Identify the blood parasite species.
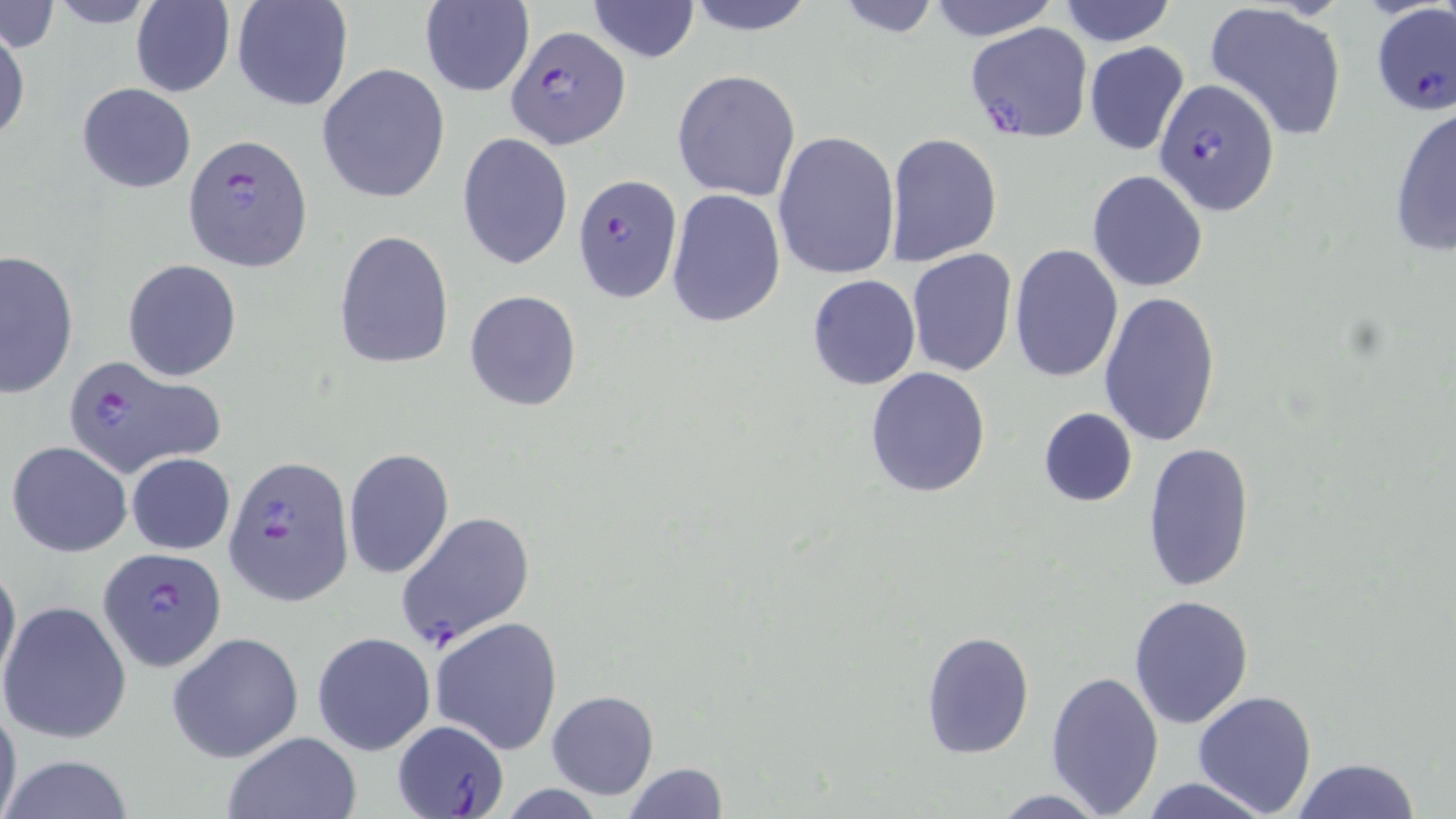

Plasmodium falciparum.

preparation = thin blood smear
Plasmodium falciparum-infected red blood cell locations = approximate bounding boxes as named x1/y1/x2/y2 corners in pixels: (x1=1370, y1=3, x2=1456, y2=116), (x1=964, y1=21, x2=1092, y2=143), (x1=506, y1=26, x2=631, y2=150), (x1=1154, y1=77, x2=1281, y2=215), (x1=180, y1=134, x2=314, y2=270), (x1=573, y1=174, x2=682, y2=301), (x1=61, y1=352, x2=222, y2=477), (x1=223, y1=455, x2=354, y2=605), (x1=394, y1=511, x2=535, y2=650), (x1=99, y1=546, x2=227, y2=672), (x1=394, y1=718, x2=508, y2=817)
modality = optical microscopy
image size = 1456×819 pixels
magnification = 1000x
uninfected red blood cell locations = approximate bounding boxes as named x1/y1/x2/y2 corners in pixels: (x1=39, y1=0, x2=164, y2=29), (x1=131, y1=0, x2=234, y2=97), (x1=229, y1=0, x2=353, y2=113), (x1=680, y1=0, x2=818, y2=36), (x1=419, y1=1, x2=534, y2=98), (x1=585, y1=1, x2=701, y2=63), (x1=924, y1=1, x2=1061, y2=42), (x1=1054, y1=1, x2=1180, y2=48), (x1=827, y1=2, x2=947, y2=37), (x1=0, y1=3, x2=59, y2=52), (x1=1203, y1=3, x2=1350, y2=142), (x1=1, y1=22, x2=28, y2=146), (x1=1084, y1=41, x2=1189, y2=156), (x1=317, y1=63, x2=450, y2=204), (x1=671, y1=69, x2=801, y2=200), (x1=77, y1=83, x2=196, y2=194), (x1=1387, y1=103, x2=1455, y2=258), (x1=773, y1=129, x2=901, y2=281), (x1=457, y1=132, x2=574, y2=270), (x1=883, y1=133, x2=1002, y2=267), (x1=1088, y1=170, x2=1208, y2=291), (x1=666, y1=188, x2=785, y2=329), (x1=334, y1=229, x2=455, y2=371), (x1=1009, y1=244, x2=1123, y2=381), (x1=0, y1=248, x2=78, y2=399), (x1=906, y1=248, x2=1017, y2=377), (x1=122, y1=259, x2=242, y2=382), (x1=806, y1=275, x2=921, y2=390), (x1=463, y1=291, x2=583, y2=411), (x1=1099, y1=291, x2=1219, y2=447), (x1=864, y1=366, x2=993, y2=500), (x1=1036, y1=407, x2=1137, y2=508), (x1=6, y1=440, x2=132, y2=558), (x1=1141, y1=442, x2=1256, y2=592), (x1=343, y1=446, x2=453, y2=581), (x1=127, y1=452, x2=234, y2=554), (x1=0, y1=556, x2=21, y2=695), (x1=1129, y1=593, x2=1255, y2=729), (x1=1, y1=599, x2=133, y2=745), (x1=431, y1=616, x2=564, y2=754), (x1=919, y1=630, x2=1035, y2=759), (x1=313, y1=631, x2=435, y2=756), (x1=167, y1=632, x2=305, y2=763), (x1=1046, y1=669, x2=1164, y2=813), (x1=546, y1=690, x2=660, y2=799), (x1=1192, y1=690, x2=1318, y2=817), (x1=0, y1=695, x2=22, y2=819), (x1=223, y1=731, x2=363, y2=819), (x1=0, y1=755, x2=138, y2=818), (x1=1290, y1=758, x2=1423, y2=818), (x1=622, y1=762, x2=727, y2=818), (x1=1136, y1=776, x2=1280, y2=818), (x1=986, y1=789, x2=1116, y2=818)
stain = May-Grünwald-Giemsa
field of view = single